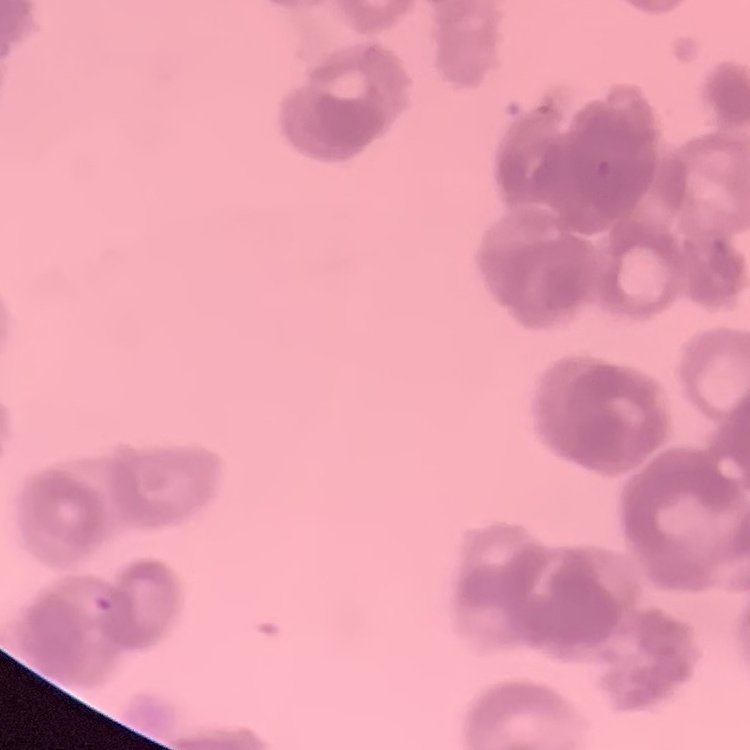

The red blood cells exhibit rouleaux formation. Stained with either Field's or Giemsa. Square crop of a larger photomicrograph. Thin peripheral smear.